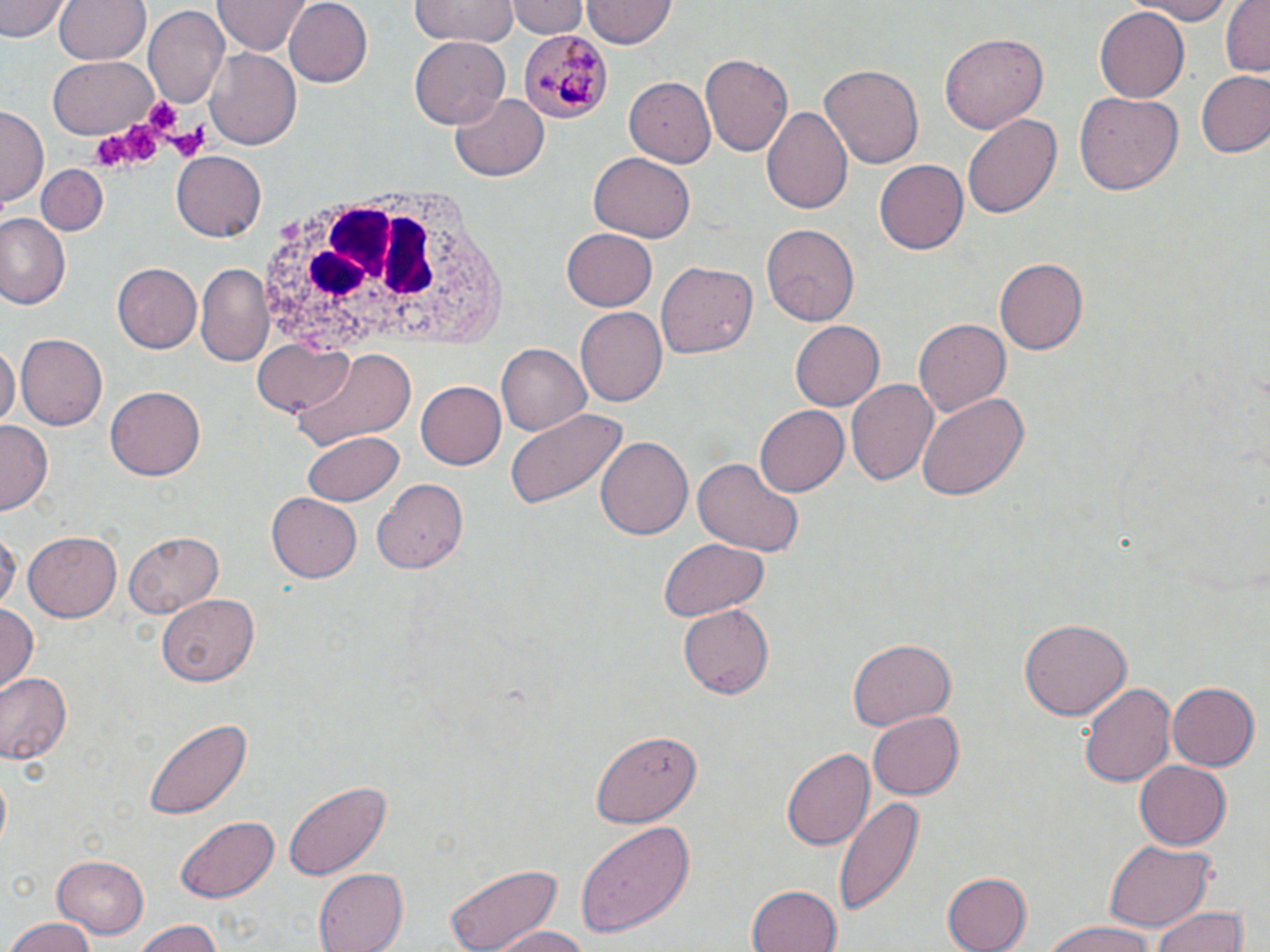
slide-level diagnosis = Plasmodium malariae
uninfected red blood cell locations = approximate bounding boxes as [x1, y1, x2, y2] in pixels: [0, 0, 68, 42], [55, 0, 149, 66], [282, 0, 372, 88], [410, 0, 515, 47], [509, 0, 586, 38], [582, 0, 675, 49], [1123, 0, 1239, 24], [1219, 0, 1270, 77], [214, 1, 307, 55], [1094, 7, 1191, 102], [143, 8, 227, 111], [940, 33, 1047, 135], [408, 36, 510, 128], [206, 48, 301, 149], [703, 51, 794, 156], [50, 56, 156, 140], [821, 63, 925, 170], [1197, 71, 1270, 157], [625, 76, 719, 165], [450, 91, 548, 181], [1075, 92, 1185, 195], [763, 106, 852, 216], [0, 107, 45, 209], [961, 113, 1062, 220], [170, 153, 265, 240], [588, 153, 694, 244], [875, 161, 969, 254], [35, 164, 108, 236], [0, 214, 69, 311], [762, 223, 863, 322], [562, 226, 658, 309], [994, 257, 1087, 355], [656, 260, 757, 358], [113, 262, 205, 353], [195, 265, 272, 365], [577, 306, 667, 408], [913, 317, 1009, 418], [789, 322, 882, 410], [16, 334, 107, 429], [252, 337, 354, 416], [0, 342, 18, 429], [497, 344, 591, 437], [294, 348, 415, 451], [846, 378, 938, 485], [416, 381, 507, 469], [106, 387, 204, 480], [915, 392, 1030, 501], [754, 405, 849, 497], [504, 407, 628, 512], [0, 422, 51, 512], [301, 429, 404, 507], [596, 435, 692, 542], [691, 458, 805, 557], [370, 481, 466, 574], [265, 493, 361, 582], [1, 529, 19, 614], [24, 532, 122, 621], [124, 533, 224, 616], [656, 538, 768, 619], [157, 595, 259, 687], [0, 603, 39, 694], [677, 604, 774, 699], [1020, 616, 1129, 719], [847, 638, 954, 731], [0, 671, 72, 765], [1082, 681, 1177, 788], [1167, 682, 1258, 772], [865, 712, 963, 798], [144, 717, 249, 819], [591, 730, 699, 826], [781, 746, 875, 850], [1132, 760, 1230, 851], [283, 781, 391, 879], [835, 794, 923, 917], [174, 815, 280, 903], [576, 820, 695, 939], [1104, 841, 1215, 929], [53, 856, 149, 938], [443, 860, 564, 951], [312, 869, 405, 952], [939, 871, 1030, 952], [745, 882, 842, 952], [1151, 908, 1250, 952], [3, 917, 98, 952], [131, 919, 223, 952], [1041, 921, 1154, 952], [491, 925, 596, 952]
stain = May-Grünwald-Giemsa
Plasmodium malariae-infected red blood cell locations = approximate bounding boxes as [x1, y1, x2, y2] in pixels: [517, 28, 611, 125]
field of view = one of a larger specimen
preparation = thin blood smear
magnification = 1000x
white blood cell locations = approximate bounding boxes as [x1, y1, x2, y2] in pixels: [252, 180, 511, 369]
platelet locations = approximate bounding boxes as [x1, y1, x2, y2] in pixels: [142, 95, 188, 139], [123, 121, 161, 163], [164, 122, 210, 163], [91, 131, 130, 170]
modality = optical microscopy
image size = 1270×952 pixels